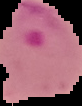

image size = 82×106 pixels
preparation = thin blood film
result = malaria parasites identified
image type = segmented cell region on a black background